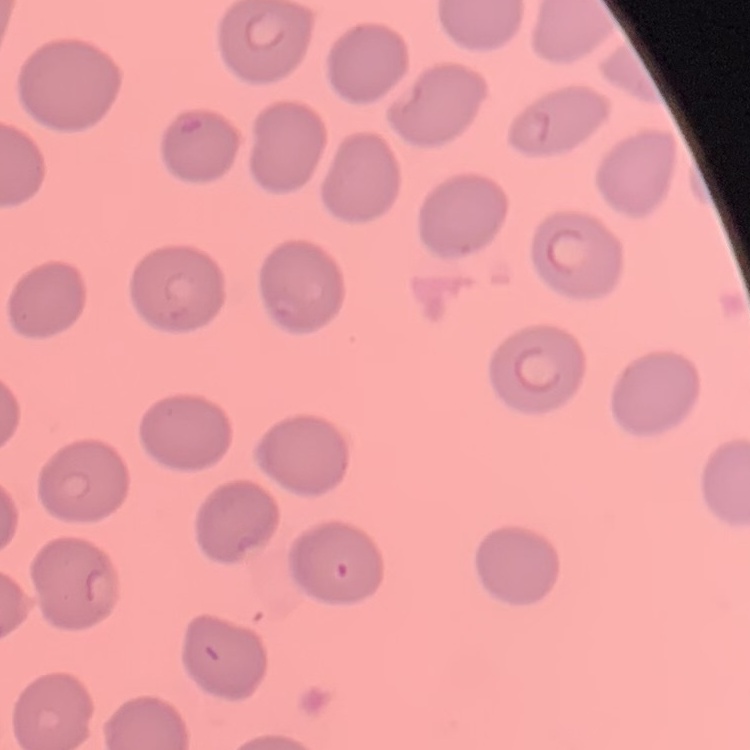

Summary:
  - Red blood cell morphology: no rouleaux formation
  - Preparation: thin blood film
  - Image type: square crop of a larger photomicrograph
  - Stain: Field's or Giemsa